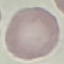

Summary:
  - Malaria status: uninfected
  - Capture: smartphone camera at the microscope eyepiece
  - Preparation: thin blood film
  - Stain: Giemsa
  - Image type: cell patch, automatically extracted from a larger field of view and resized to 64 × 64 pixels